Describe the morphology of the erythrocytes.
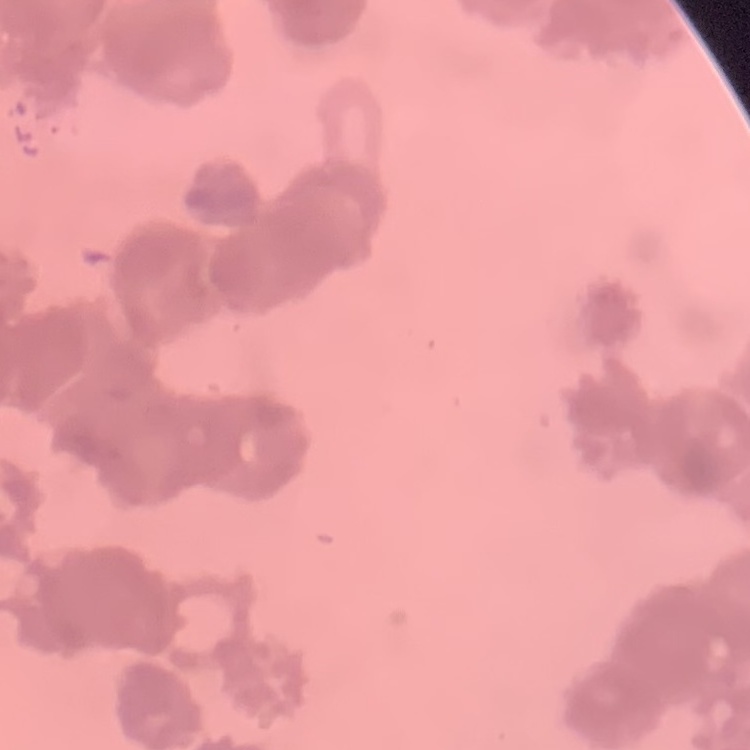
They show rouleaux formation.

Square crop of a larger photomicrograph. Stained with either Field's or Giemsa. Thin blood smear.